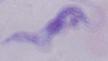 Captured at 1000x magnification. A trypanosome is shown. Photomicrograph.